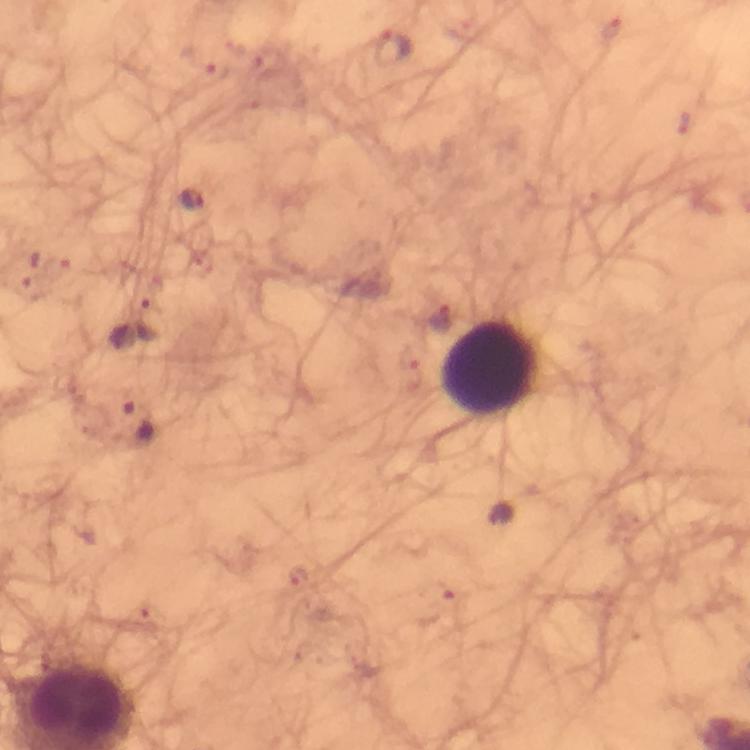

Approximate centers as (x, y) in pixels. Leukocyte locations: (488, 367). Plasmodium parasite locations: (393, 48), (191, 200), (31, 270), (152, 319), (137, 423). Image is 750×750 pixels. Giemsa-stained preparation. Cropped region of a single field of view. From a malaria diagnostic workup. Thick blood film. Smartphone photograph taken through a microscope. At 100x magnification. Immersion oil was used.